Report the malaria status of this cell.
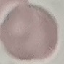
Uninfected.

Cell patch, automatically extracted from a larger field of view and resized to 64 × 64 pixels. Giemsa stain. Thin blood film. Photographed with a smartphone camera at the microscope eyepiece.